Assess the morphology of the red blood cells.
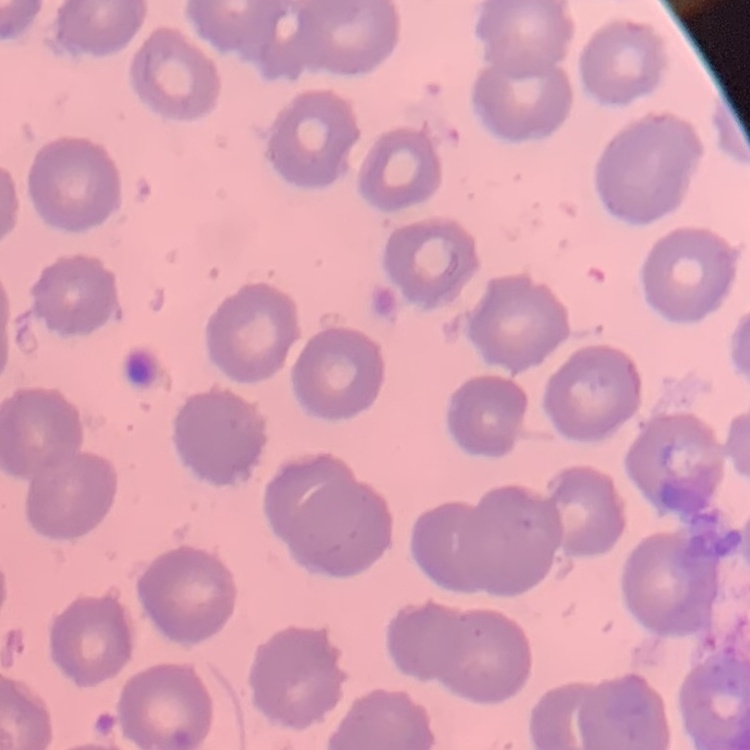
No rouleaux formation.

Thin peripheral smear. Field's or Giemsa stain. One tile cut from a larger photomicrograph.